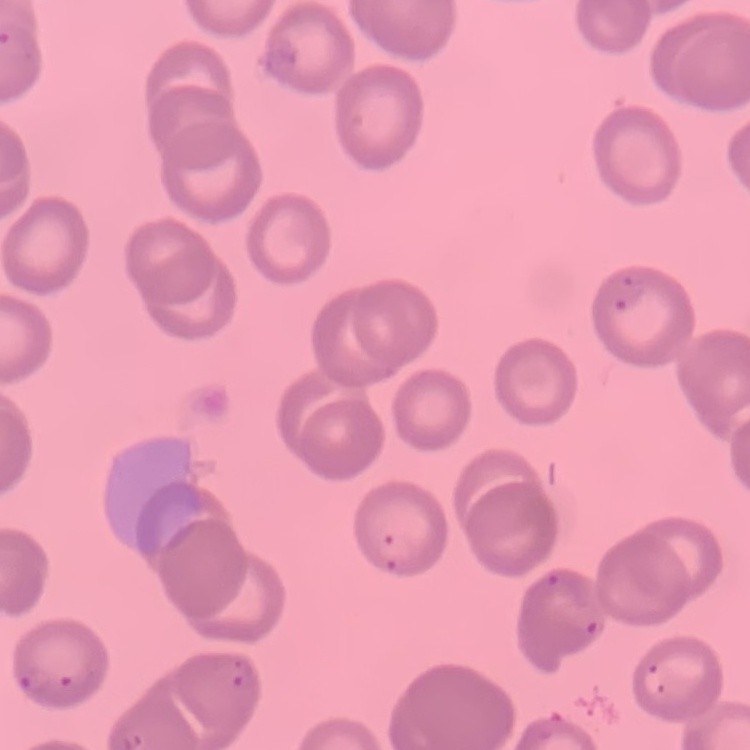
Summary:
  - Red blood cell morphology: no rouleaux formation
  - Image type: square crop of a larger photomicrograph
  - Stain: Field's or Giemsa
  - Preparation: thin peripheral smear